Give the preparation type.
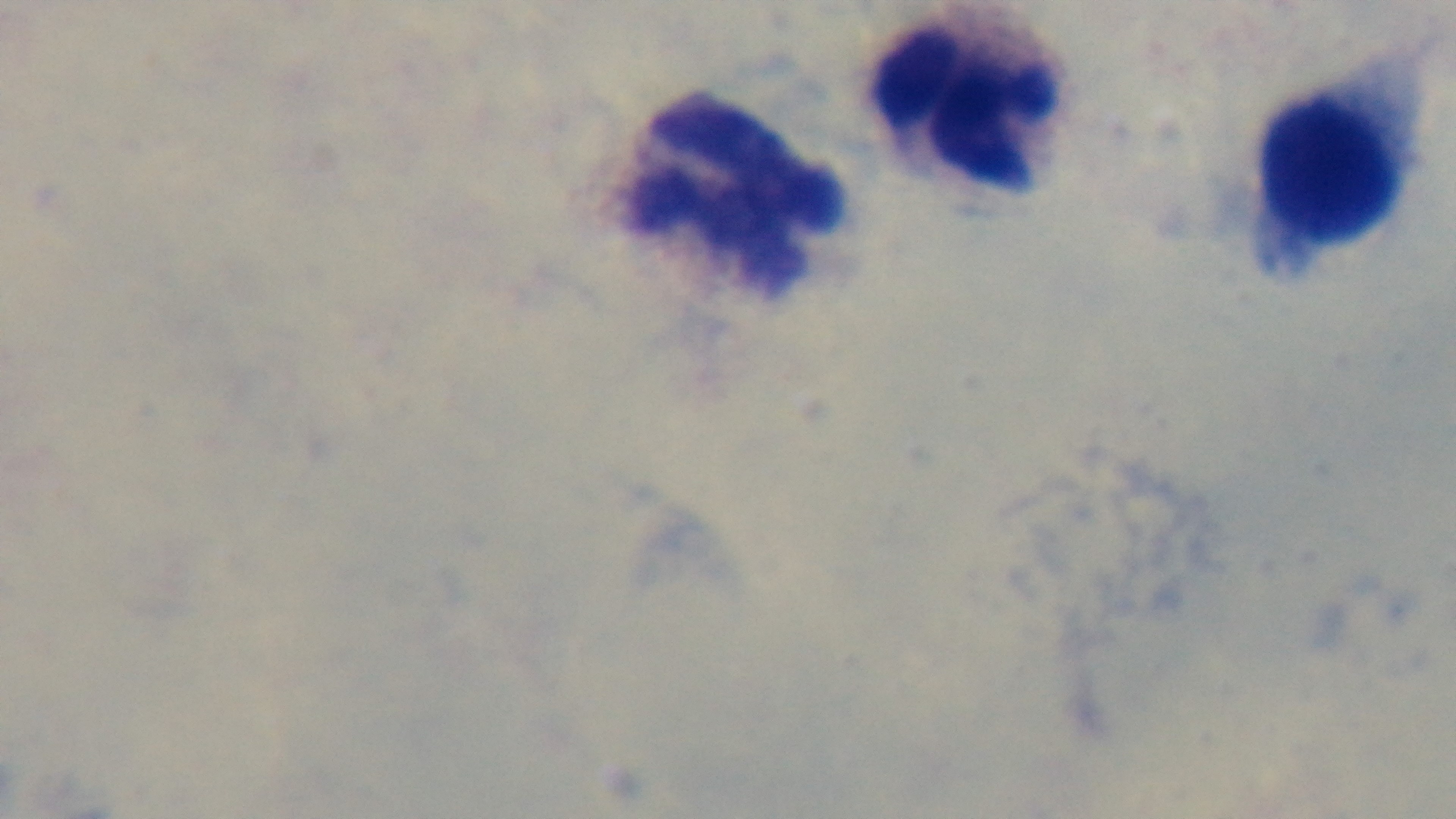
A thick smear.

malaria status = uninfected
capture = mounted 4K digital camera
objective = 100x oil immersion
field of view = single
stain = Giemsa
modality = light microscopy